Point out every malaria parasite and every leukocyte.
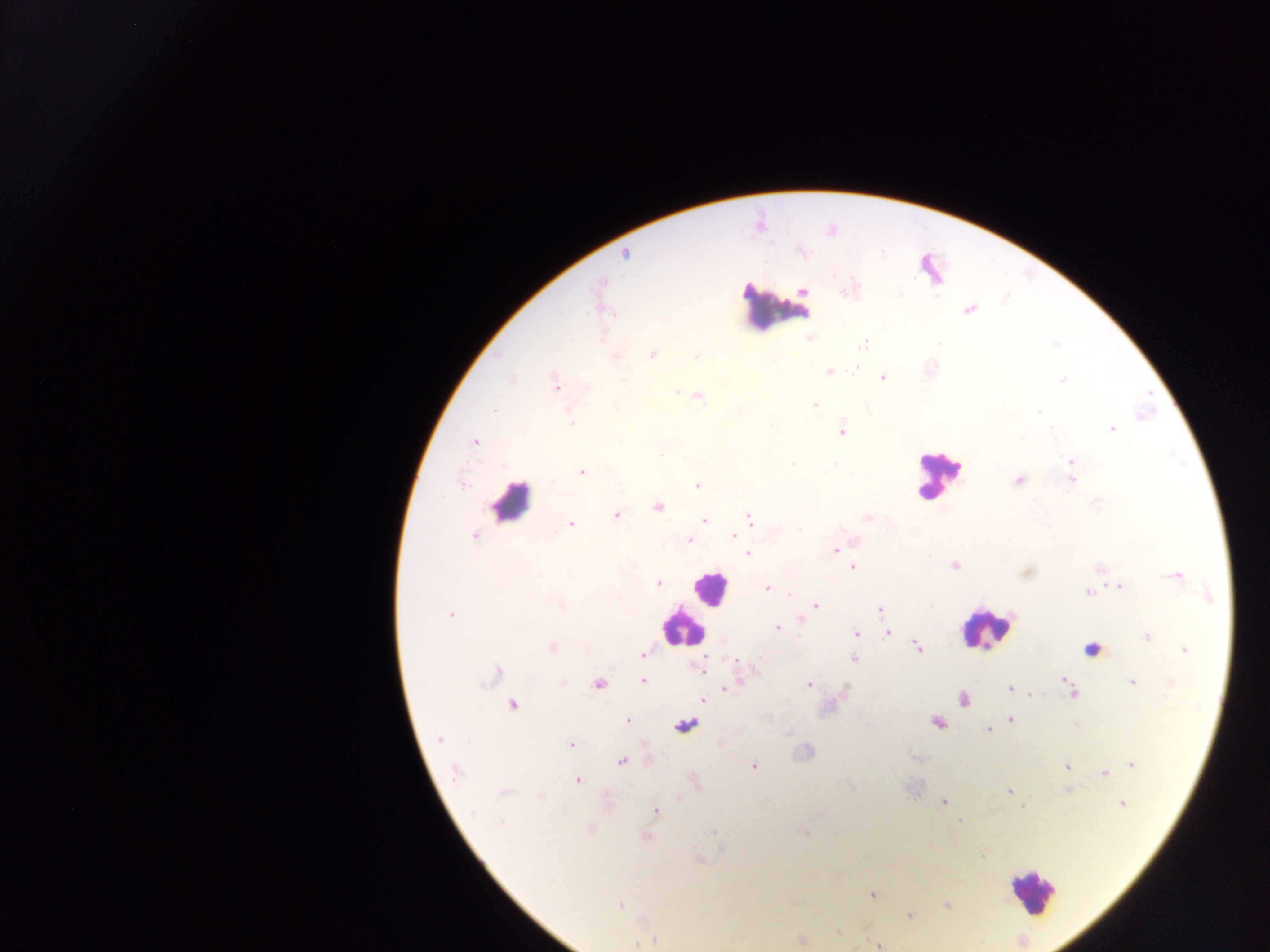
Approximate centers as {x, y} in pixels.
Malaria parasites: {625, 254}, {600, 282}, {804, 291}, {850, 291}, {968, 310}, {808, 338}, {864, 343}, {653, 355}, {696, 356}, {616, 357}, {856, 367}, {829, 372}, {883, 378}, {511, 379}, {1062, 381}, {555, 382}, {675, 391}, {699, 397}, {814, 405}, {494, 410}, {1038, 412}, {572, 423}, {1112, 429}, {842, 432}, {474, 442}, {660, 453}, {1071, 461}, {792, 464}, {835, 465}, {581, 471}, {1071, 479}, {1019, 480}, {462, 484}, {697, 485}, {658, 507}, {617, 516}, {868, 517}, {749, 518}, {704, 520}, {571, 524}, {800, 530}, {734, 536}, {475, 537}, {689, 540}, {835, 549}, {747, 553}, {954, 565}, {853, 568}, {1174, 576}, {658, 583}, {1119, 587}, {767, 588}, {1088, 592}, {560, 604}, {815, 605}, {880, 610}, {450, 615}, {801, 619}, {777, 628}, {888, 632}, {856, 634}, {1147, 636}, {918, 647}, {552, 648}, {1185, 650}, {643, 655}, {854, 658}, {735, 659}, {701, 669}, {494, 676}, {644, 681}, {563, 682}, {1067, 682}, {1132, 683}, {1171, 683}, {599, 685}, {809, 685}, {727, 687}, {1010, 688}, {1073, 692}, {1031, 695}, {702, 699}, {964, 700}, {512, 705}, {628, 720}, {1011, 720}, {937, 722}, {987, 730}, {439, 739}, {571, 744}, {621, 760}, {1132, 765}, {753, 766}, {1066, 766}, {456, 771}, {1104, 773}, {578, 780}, {1009, 791}, {503, 793}, {943, 802}, {1122, 804}, {1022, 807}, {655, 809}, {960, 821}, {591, 829}, {712, 832}, {647, 837}, {982, 856}, {700, 860}, {872, 894}, {620, 905}, {947, 905}, {910, 915}, {837, 932}, {801, 939}, {652, 941}, {637, 943}, {878, 945}.
Leukocytes: {777, 307}, {937, 475}, {510, 503}, {709, 587}, {682, 626}, {986, 629}, {1092, 644}, {686, 727}, {1031, 891}.

{
  "image_size": "1270×952 pixels",
  "country": "Ghana",
  "preparation": "thick blood smear",
  "capture": "mobile-phone photograph through a microscope",
  "field_of_view": "single"
}